Describe the morphology of the erythrocytes.
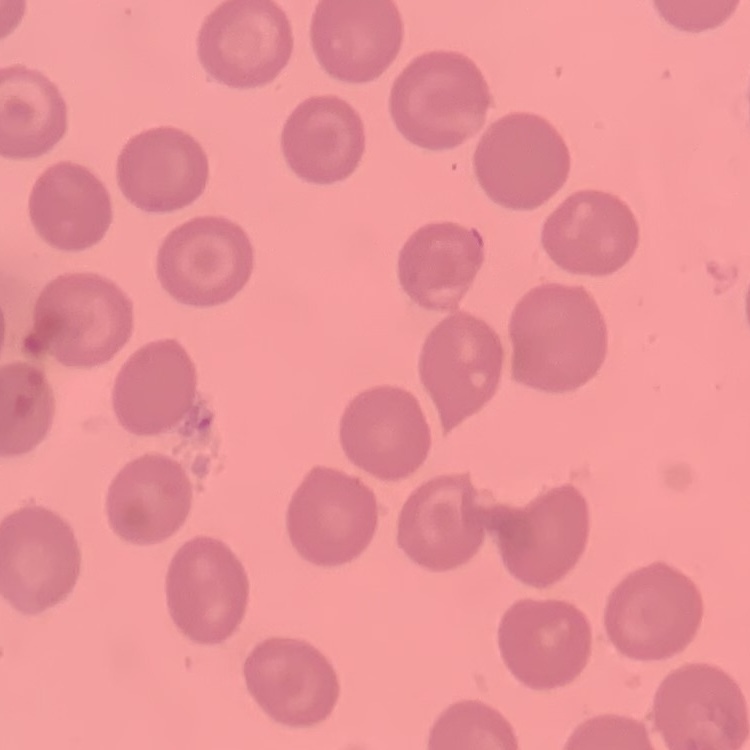
They show no rouleaux formation.

Thin blood smear. Square crop of a larger photomicrograph. Field's or Giemsa stain.